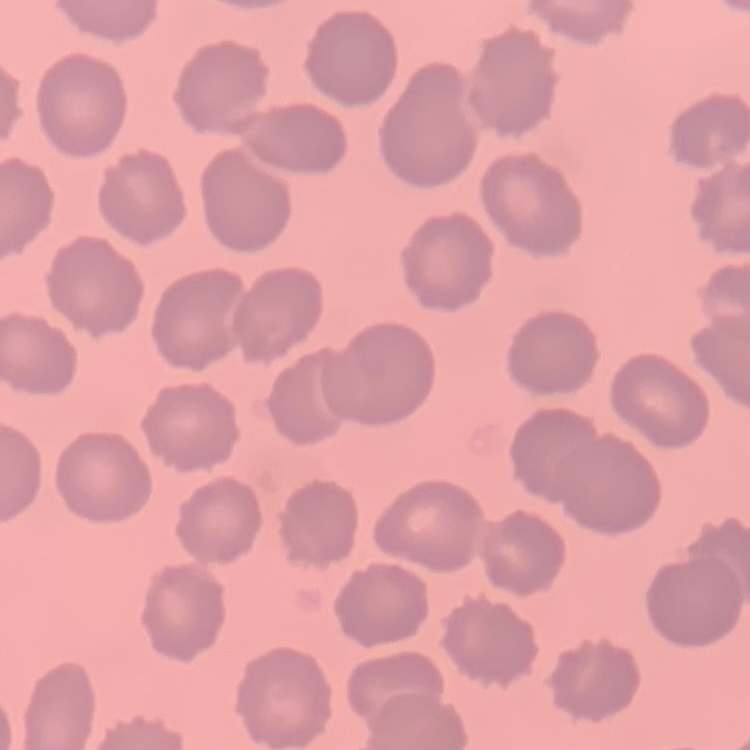
Summary:
  - Red blood cell morphology: no rouleaux formation
  - Image type: one tile cut from a larger photomicrograph
  - Preparation: thin peripheral smear
  - Stain: Field's or Giemsa